Identify the blood parasite species.
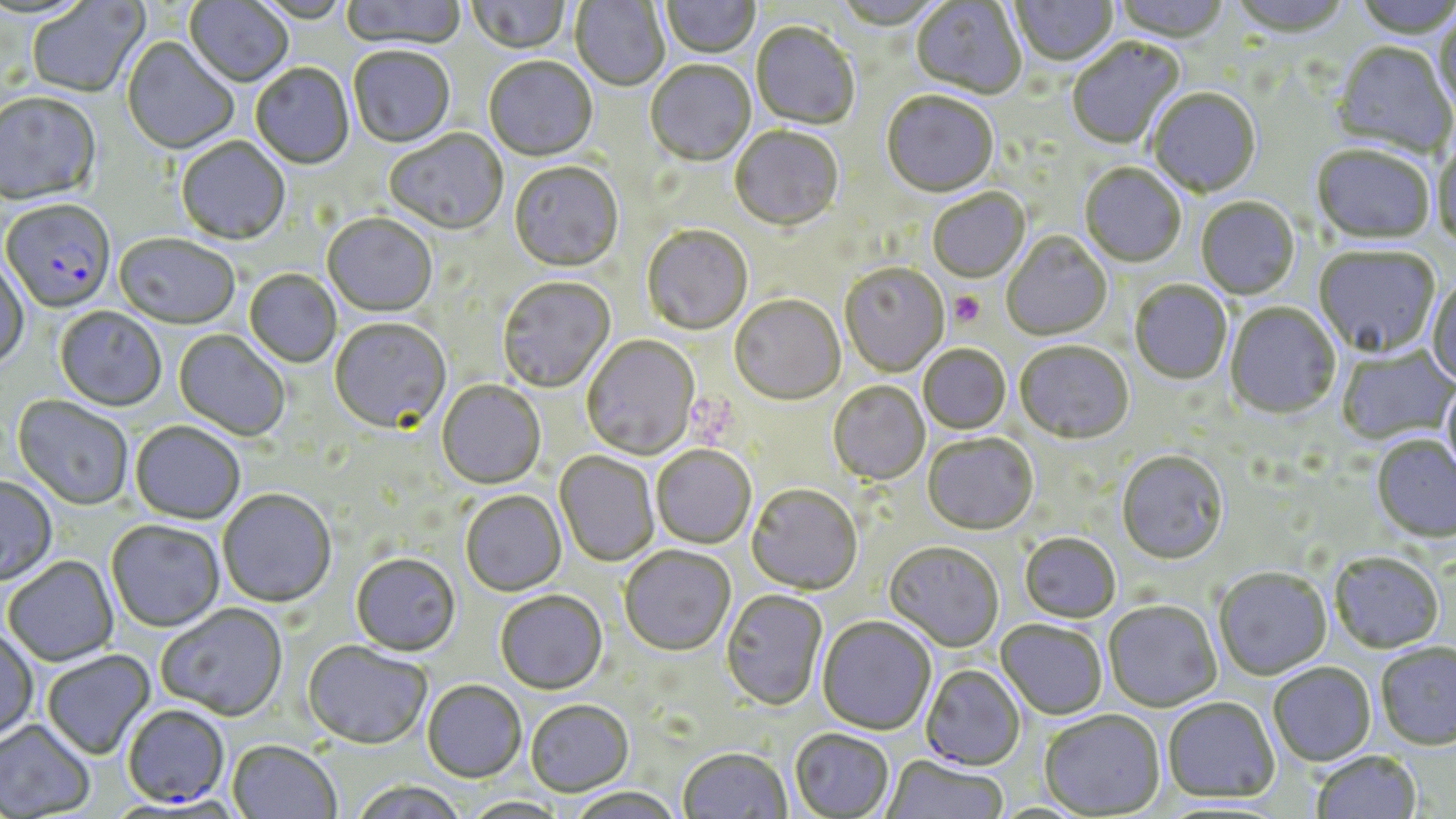

Plasmodium falciparum.

Approximate bounding boxes as named x1/y1/x2/y2 corners in pixels. Platelet locations: (x1=949, y1=292, x2=986, y2=327). Plasmodium falciparum-infected red blood cell locations: (x1=2, y1=201, x2=116, y2=314), (x1=122, y1=706, x2=230, y2=809). Uninfected red blood cell locations: (x1=25, y1=0, x2=150, y2=100), (x1=340, y1=0, x2=466, y2=51), (x1=569, y1=0, x2=670, y2=92), (x1=831, y1=0, x2=947, y2=32), (x1=1010, y1=0, x2=1119, y2=68), (x1=1110, y1=0, x2=1230, y2=45), (x1=1226, y1=0, x2=1354, y2=40), (x1=1351, y1=0, x2=1456, y2=40), (x1=184, y1=1, x2=293, y2=88), (x1=465, y1=1, x2=573, y2=56), (x1=661, y1=1, x2=761, y2=60), (x1=911, y1=1, x2=1027, y2=101), (x1=1434, y1=12, x2=1456, y2=118), (x1=750, y1=24, x2=860, y2=131), (x1=122, y1=38, x2=239, y2=156), (x1=1067, y1=38, x2=1185, y2=150), (x1=1330, y1=43, x2=1455, y2=160), (x1=348, y1=48, x2=455, y2=149), (x1=484, y1=58, x2=597, y2=163), (x1=645, y1=61, x2=756, y2=168), (x1=251, y1=64, x2=355, y2=170), (x1=1148, y1=89, x2=1261, y2=199), (x1=0, y1=93, x2=102, y2=209), (x1=881, y1=93, x2=999, y2=200), (x1=730, y1=127, x2=844, y2=233), (x1=384, y1=130, x2=508, y2=237), (x1=176, y1=138, x2=290, y2=246), (x1=1432, y1=138, x2=1456, y2=251), (x1=1311, y1=147, x2=1435, y2=246), (x1=509, y1=163, x2=623, y2=274), (x1=1079, y1=165, x2=1185, y2=269), (x1=928, y1=190, x2=1030, y2=284), (x1=1196, y1=198, x2=1300, y2=300), (x1=323, y1=214, x2=437, y2=318), (x1=642, y1=226, x2=753, y2=337), (x1=1002, y1=233, x2=1112, y2=342), (x1=114, y1=235, x2=240, y2=331), (x1=1314, y1=248, x2=1440, y2=359), (x1=0, y1=260, x2=29, y2=370), (x1=840, y1=264, x2=949, y2=377), (x1=244, y1=270, x2=342, y2=368), (x1=1427, y1=274, x2=1456, y2=389), (x1=497, y1=278, x2=616, y2=394), (x1=1130, y1=281, x2=1232, y2=385), (x1=730, y1=296, x2=846, y2=407), (x1=1225, y1=303, x2=1341, y2=420), (x1=55, y1=308, x2=167, y2=412), (x1=330, y1=319, x2=451, y2=435), (x1=173, y1=330, x2=290, y2=442), (x1=582, y1=336, x2=700, y2=460), (x1=1015, y1=343, x2=1134, y2=446), (x1=918, y1=346, x2=1011, y2=435), (x1=1336, y1=347, x2=1456, y2=446), (x1=1441, y1=377, x2=1456, y2=486), (x1=437, y1=381, x2=546, y2=490), (x1=828, y1=382, x2=930, y2=486), (x1=12, y1=397, x2=134, y2=511), (x1=130, y1=423, x2=245, y2=525), (x1=922, y1=435, x2=1038, y2=536), (x1=1371, y1=436, x2=1455, y2=543), (x1=651, y1=446, x2=756, y2=549), (x1=555, y1=451, x2=660, y2=567), (x1=1116, y1=452, x2=1228, y2=565), (x1=0, y1=477, x2=57, y2=587), (x1=746, y1=486, x2=863, y2=596), (x1=218, y1=490, x2=337, y2=609), (x1=460, y1=491, x2=566, y2=597), (x1=106, y1=521, x2=225, y2=633), (x1=1019, y1=534, x2=1121, y2=624), (x1=884, y1=543, x2=1004, y2=652), (x1=619, y1=548, x2=736, y2=658), (x1=1329, y1=551, x2=1444, y2=653), (x1=351, y1=555, x2=462, y2=658), (x1=3, y1=556, x2=119, y2=667), (x1=1213, y1=568, x2=1331, y2=680), (x1=720, y1=590, x2=828, y2=712), (x1=495, y1=592, x2=607, y2=696), (x1=1103, y1=601, x2=1221, y2=712), (x1=156, y1=605, x2=288, y2=723), (x1=817, y1=617, x2=937, y2=736), (x1=996, y1=621, x2=1107, y2=720), (x1=0, y1=628, x2=39, y2=742), (x1=302, y1=642, x2=432, y2=751), (x1=1375, y1=642, x2=1456, y2=749), (x1=42, y1=650, x2=156, y2=760), (x1=1267, y1=662, x2=1376, y2=765), (x1=920, y1=665, x2=1026, y2=771), (x1=423, y1=681, x2=526, y2=783), (x1=1163, y1=697, x2=1279, y2=803), (x1=526, y1=702, x2=634, y2=798), (x1=1039, y1=710, x2=1166, y2=818), (x1=0, y1=720, x2=96, y2=817), (x1=789, y1=729, x2=894, y2=818), (x1=227, y1=741, x2=341, y2=819), (x1=678, y1=749, x2=791, y2=819), (x1=1310, y1=749, x2=1422, y2=819), (x1=881, y1=756, x2=1007, y2=818), (x1=351, y1=781, x2=468, y2=819), (x1=567, y1=789, x2=684, y2=819), (x1=460, y1=797, x2=571, y2=818). Image is 1456×819 pixels. May-Grünwald-Giemsa-stained preparation. Thin blood film. Light microscopy. 1000x magnification. One field of a larger specimen.